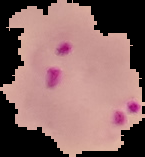
From a thin blood film. Result: malaria parasites identified. Segmented cell region on a black background. Image is 145×157 pixels.